Report the malaria status of this cell.
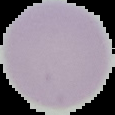
It is uninfected.

image size = 115×115 pixels
preparation = thin blood film
image type = segmented cell region with the area outside set to black